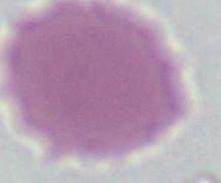

1000x magnification. A red blood cell is shown. Photomicrograph.